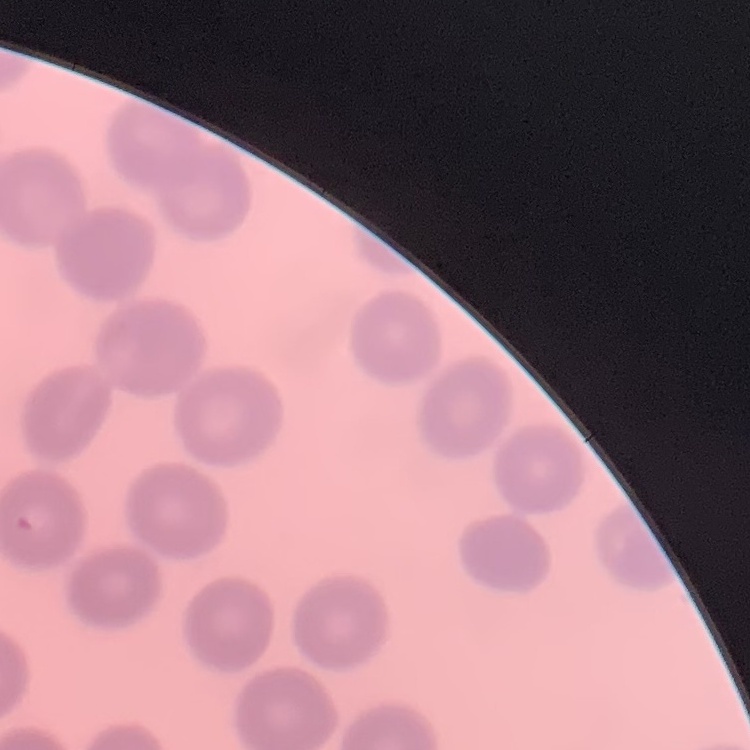

Summary:
  - Red blood cell morphology: no rouleaux formation
  - Preparation: thin blood film
  - Image type: square crop of a larger photomicrograph
  - Stain: Field's or Giemsa